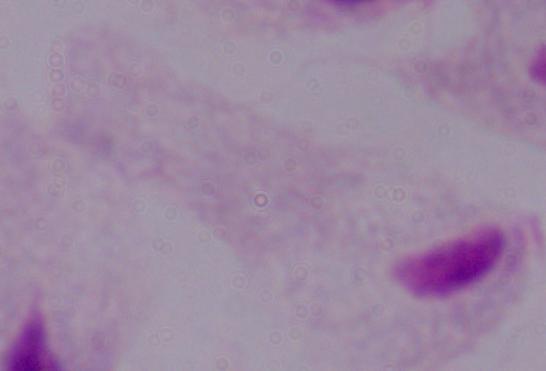
Summary:
  - Magnification: 1000x
  - Modality: micrograph
  - Identification: trichomonad